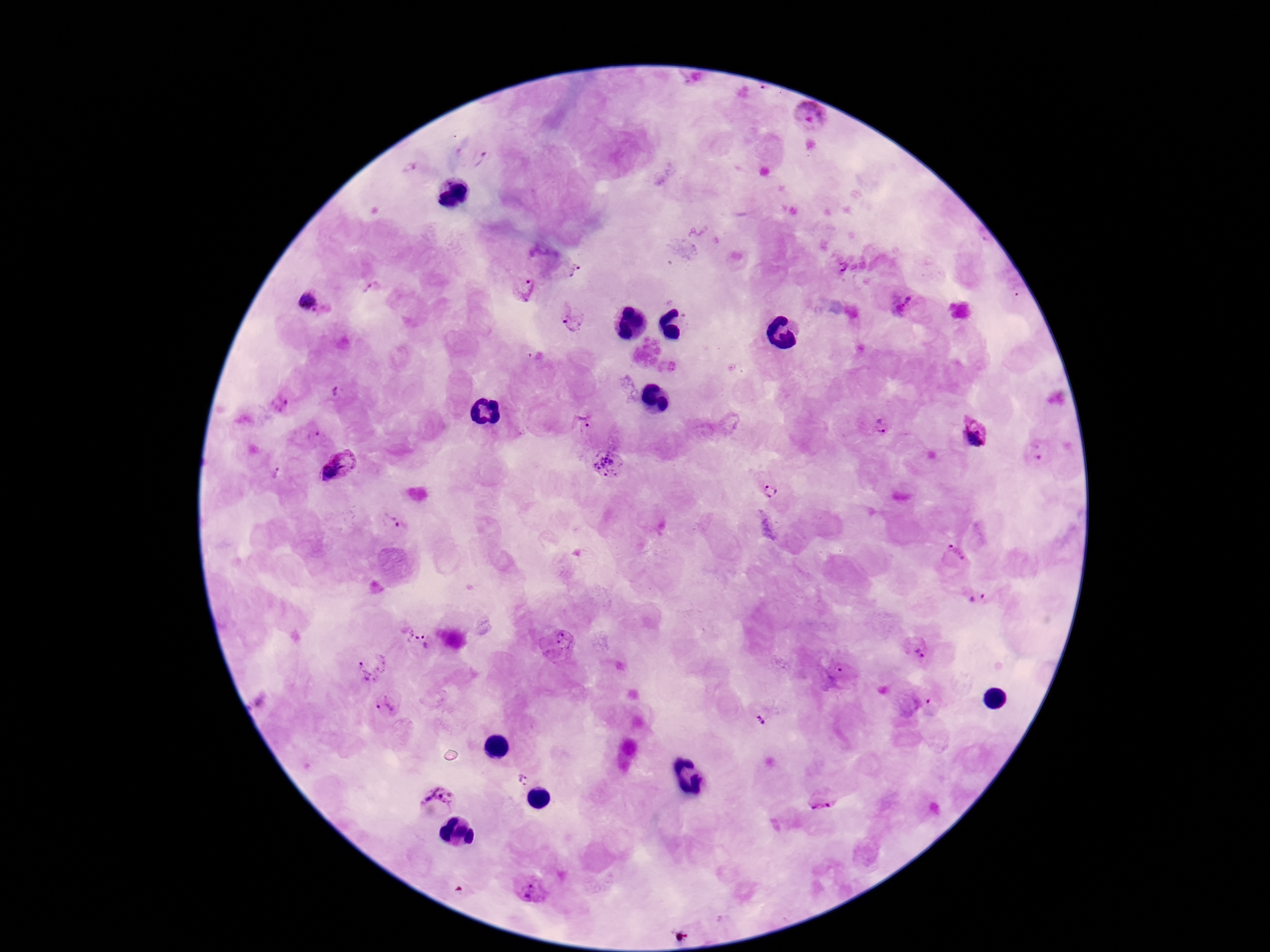
capture = smartphone camera through the microscope eyepiece
image size = 1270×952 pixels
stain = Giemsa
Plasmodium parasite locations = approximate centers as {x, y} in pixels: {808, 116}, {480, 158}, {837, 264}, {569, 267}, {371, 286}, {522, 288}, {314, 303}, {902, 305}, {569, 315}, {340, 392}, {279, 404}, {582, 420}, {875, 425}, {974, 432}, {312, 433}, {609, 463}, {338, 464}, {770, 490}, {394, 521}, {766, 528}, {956, 552}, {976, 597}, {419, 636}, {558, 644}, {916, 649}, {370, 665}, {835, 673}, {385, 706}, {761, 715}, {520, 778}, {438, 798}, {824, 799}, {529, 891}
patient malaria status = positive
magnification = 100x
preparation = thick blood smear
field of view = one from this slide